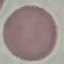 Result: no malaria parasites detected. Giemsa-stained preparation. Automatically extracted cell patch, resized to 64 × 64 pixels. Thin smear of blood. Photographed with a smartphone camera at the microscope eyepiece.